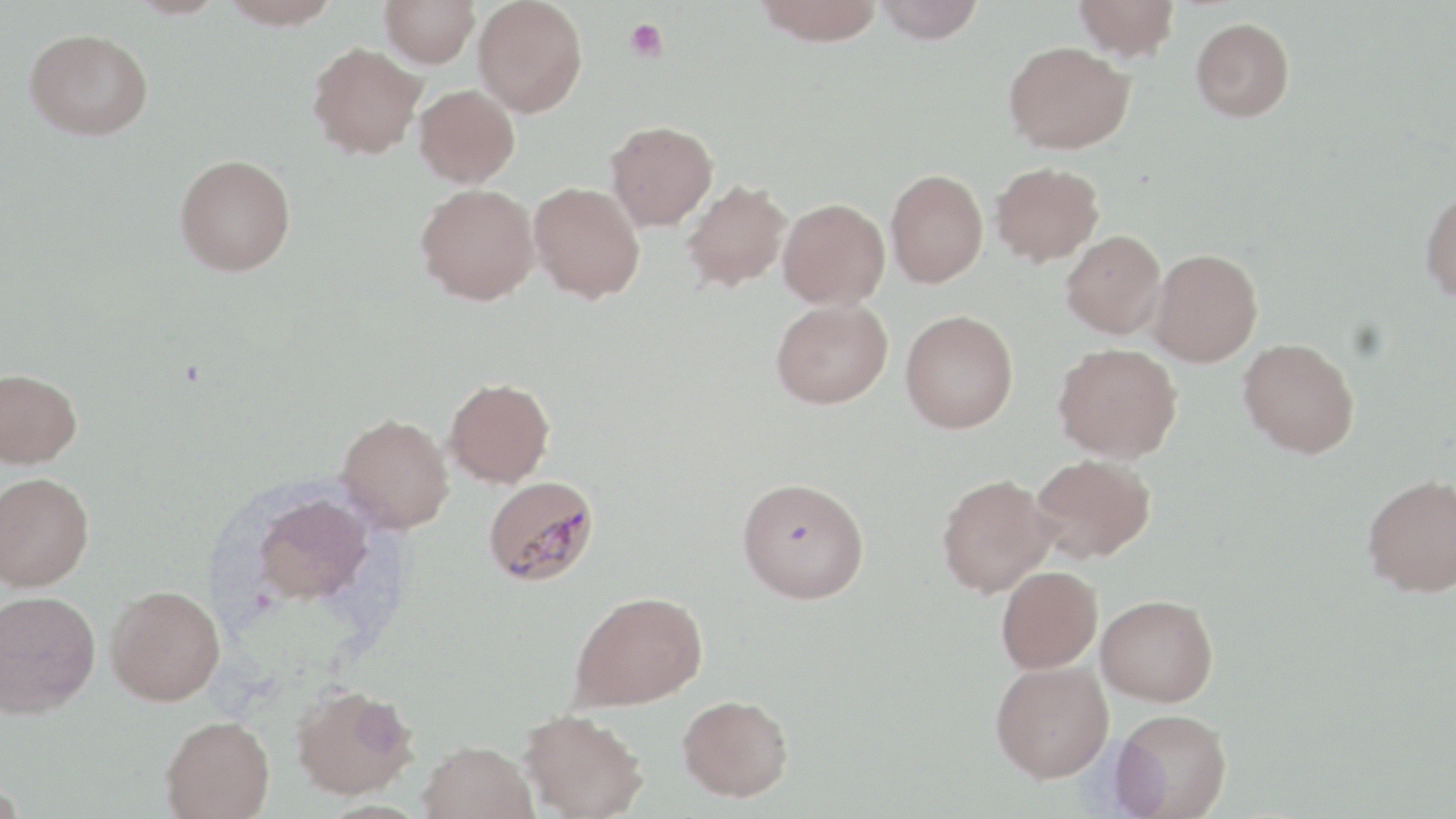

Summary:
  - Coordinate format: approximate bounding boxes as (x1,y1)-(x2,y2) corner pairs in pixels
  - Platelet locations: (625,19)-(668,63)
  - Plasmodium malariae-infected red blood cell locations: (483,475)-(599,586)
  - Uninfected red blood cell locations: (124,0)-(230,19), (219,0)-(343,29), (380,0)-(480,68), (473,0)-(587,117), (755,0)-(883,46), (873,0)-(986,43), (1074,0)-(1180,61), (1190,17)-(1295,121), (24,28)-(153,140), (1004,41)-(1134,154), (308,42)-(426,159), (414,84)-(520,187), (605,120)-(718,231), (174,154)-(296,276), (990,161)-(1104,266), (885,169)-(988,287), (681,179)-(791,292), (528,181)-(645,302), (416,183)-(539,305), (1420,187)-(1456,302), (778,197)-(890,309), (1061,230)-(1166,338), (1148,248)-(1263,367), (771,299)-(892,409), (900,310)-(1018,433), (1238,337)-(1360,457), (1053,343)-(1182,463), (0,367)-(82,468), (445,377)-(555,488), (337,413)-(454,533), (1031,454)-(1155,563), (0,472)-(94,591), (936,473)-(1056,597), (1362,473)-(1456,597), (737,477)-(869,604), (249,492)-(375,607), (996,565)-(1103,673), (106,584)-(225,706), (0,590)-(100,717), (569,590)-(707,710), (1096,594)-(1218,706), (990,660)-(1114,782), (291,683)-(418,800), (677,694)-(793,801), (519,708)-(648,819), (1111,708)-(1232,819), (161,715)-(275,818), (417,740)-(538,819)
  - Slide-level diagnosis: Plasmodium malariae
  - Preparation: thin blood smear
  - Field of view: one of a larger specimen
  - Modality: optical microscopy
  - Magnification: 1000x
  - Image size: 1456×819 pixels
  - Stain: May-Grünwald-Giemsa